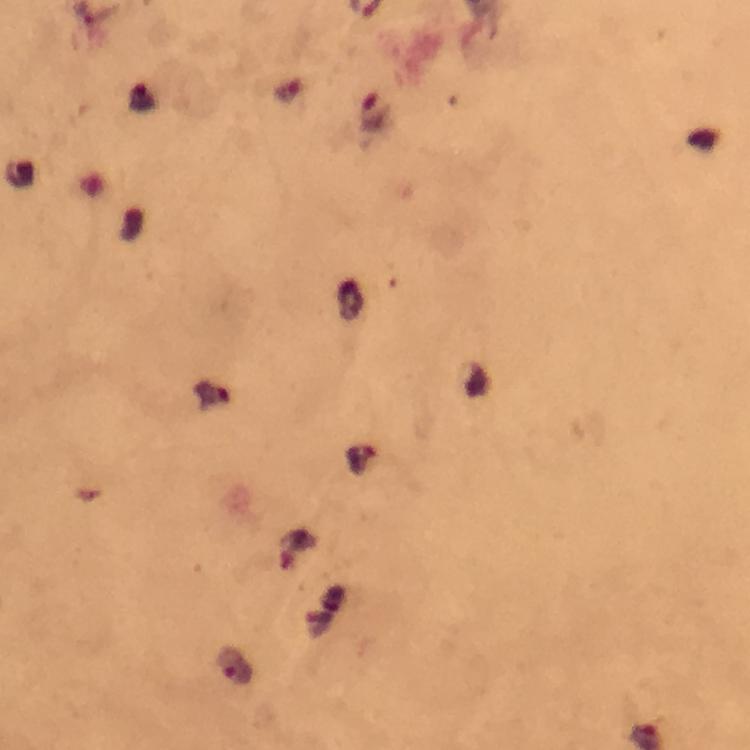

Approximate centers as {x, y} in pixels.
Summary:
  - Malaria parasite locations: {376, 114}, {360, 457}
  - Cropped from: a single field of view
  - Immersion oil: applied
  - Capture: smartphone camera through the microscope
  - Magnification: 100x
  - Context: from a diagnostic examination for malaria
  - Stain: Giemsa
  - Preparation: thick blood film
  - Image size: 750×750 pixels